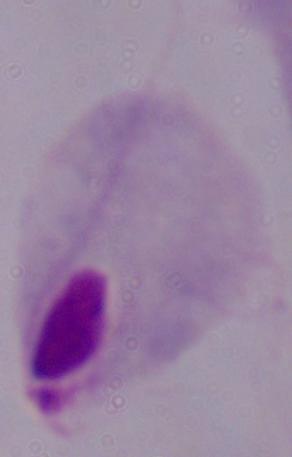

Captured at 1000x magnification. A trichomonad is shown. Photomicrograph.